Assess this cell for malaria.
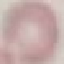

It is uninfected.

Acquired by smartphone through the microscope eyepiece. Giemsa stain. Cell patch, automatically extracted from a larger field of view and resized to 64 × 64 pixels. Thin blood smear.